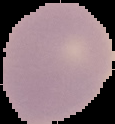

preparation: thin blood smear
image_type: segmented cell region on a black background
malaria_status: uninfected
image_size: 115×124 pixels